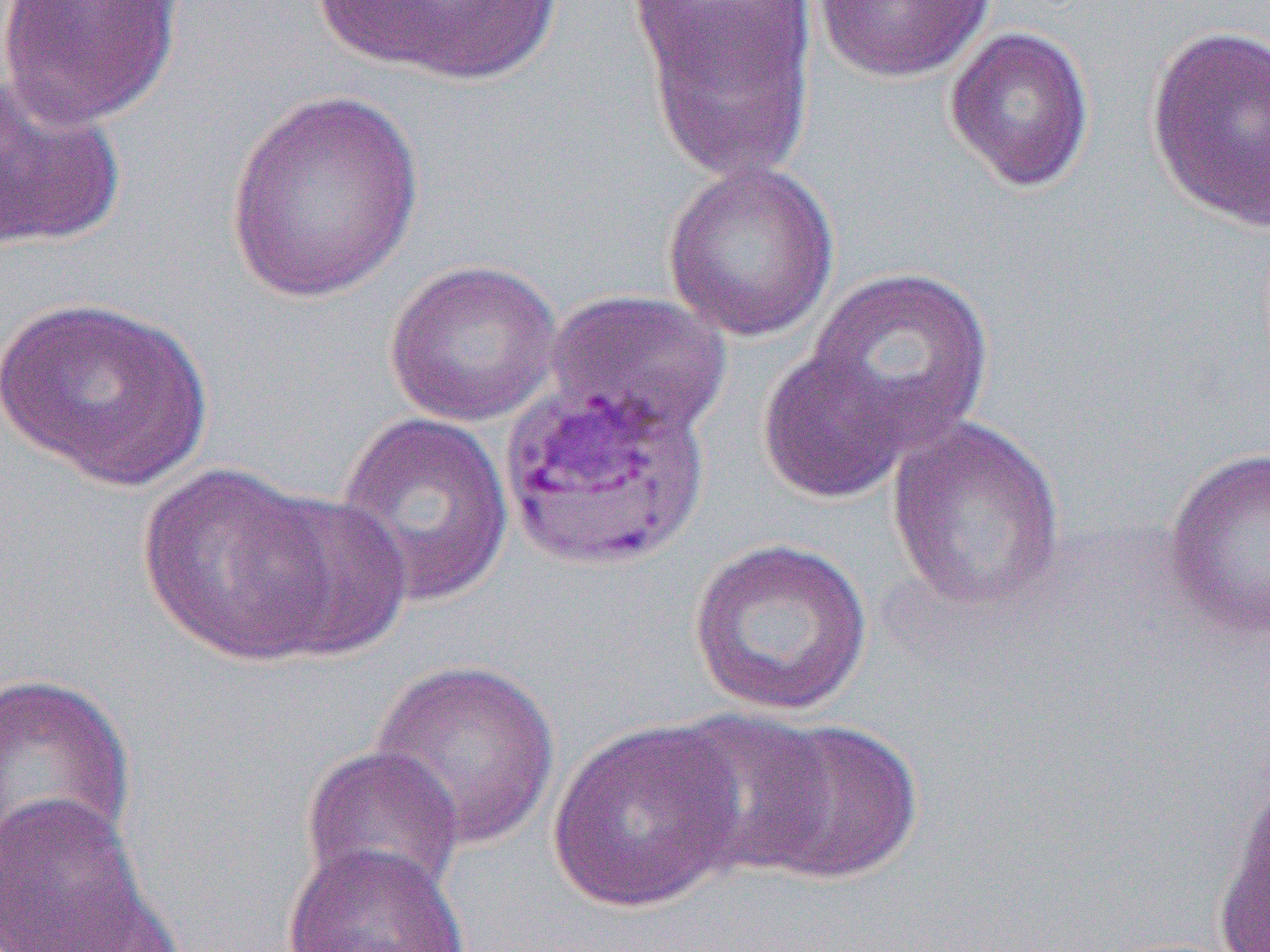

slide-level diagnosis = Plasmodium vivax
modality = optical microscopy
field of view = one of a larger specimen
image size = 1270×952 pixels
preparation = thin blood film
magnification = 1000x
uninfected red blood cell locations = approximate bounding boxes as (x1,y1)-(x2,y2) corner pairs in pixels: (0,0)-(185,129), (319,0)-(566,86), (813,0)-(997,84), (626,1)-(817,82), (629,2)-(819,181), (1144,23)-(1270,233), (943,24)-(1096,194), (0,76)-(126,251), (225,89)-(425,304), (661,159)-(840,343), (383,257)-(563,428), (805,267)-(995,455), (544,289)-(733,440), (0,295)-(213,490), (757,347)-(914,505), (334,411)-(515,608), (885,415)-(1067,614), (1161,446)-(1269,644), (137,463)-(339,666), (250,490)-(415,662), (687,536)-(875,718), (367,658)-(561,850), (1,670)-(136,871), (663,709)-(836,878), (748,718)-(923,886), (547,719)-(747,914), (303,747)-(467,901), (1211,772)-(1270,952), (0,790)-(168,952), (282,843)-(470,952), (23,878)-(187,950)